Locate every Plasmodium parasite.
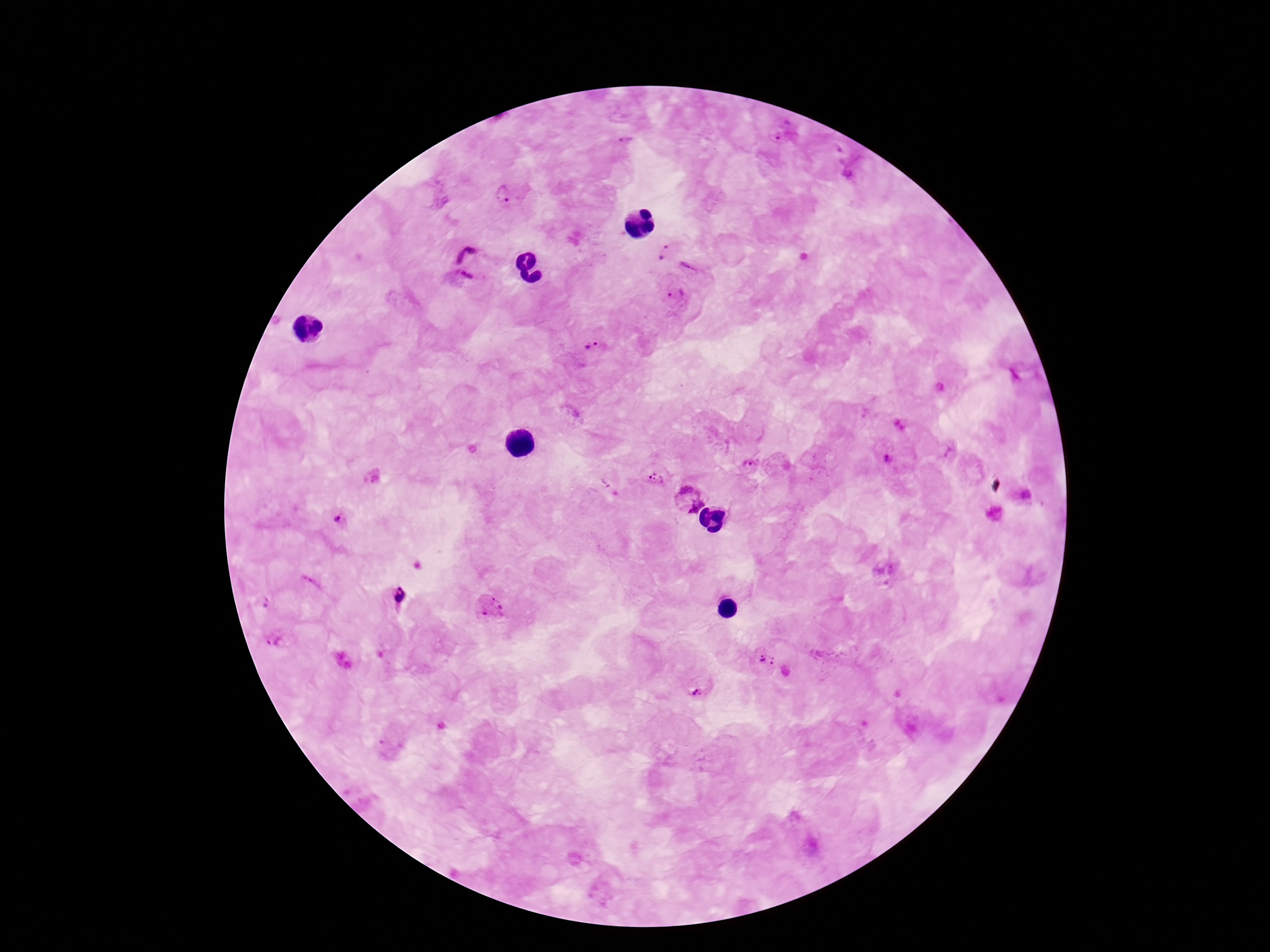
Approximate centers as (x, y) in pixels.
Plasmodium parasites: (783, 131), (626, 140), (848, 161), (502, 196), (664, 252), (471, 262), (690, 267), (679, 297), (592, 345), (888, 456), (750, 465), (655, 478), (603, 482), (1022, 495), (689, 499), (341, 523), (886, 572), (395, 598), (266, 601), (489, 607), (277, 641), (764, 658), (343, 660), (697, 688).

Summary:
  - Image size: 1270×952 pixels
  - Capture: smartphone camera through the microscope eyepiece
  - Preparation: thick blood smear
  - Magnification: 100x
  - Field of view: single
  - Patient malaria status: positive
  - Stain: Giemsa